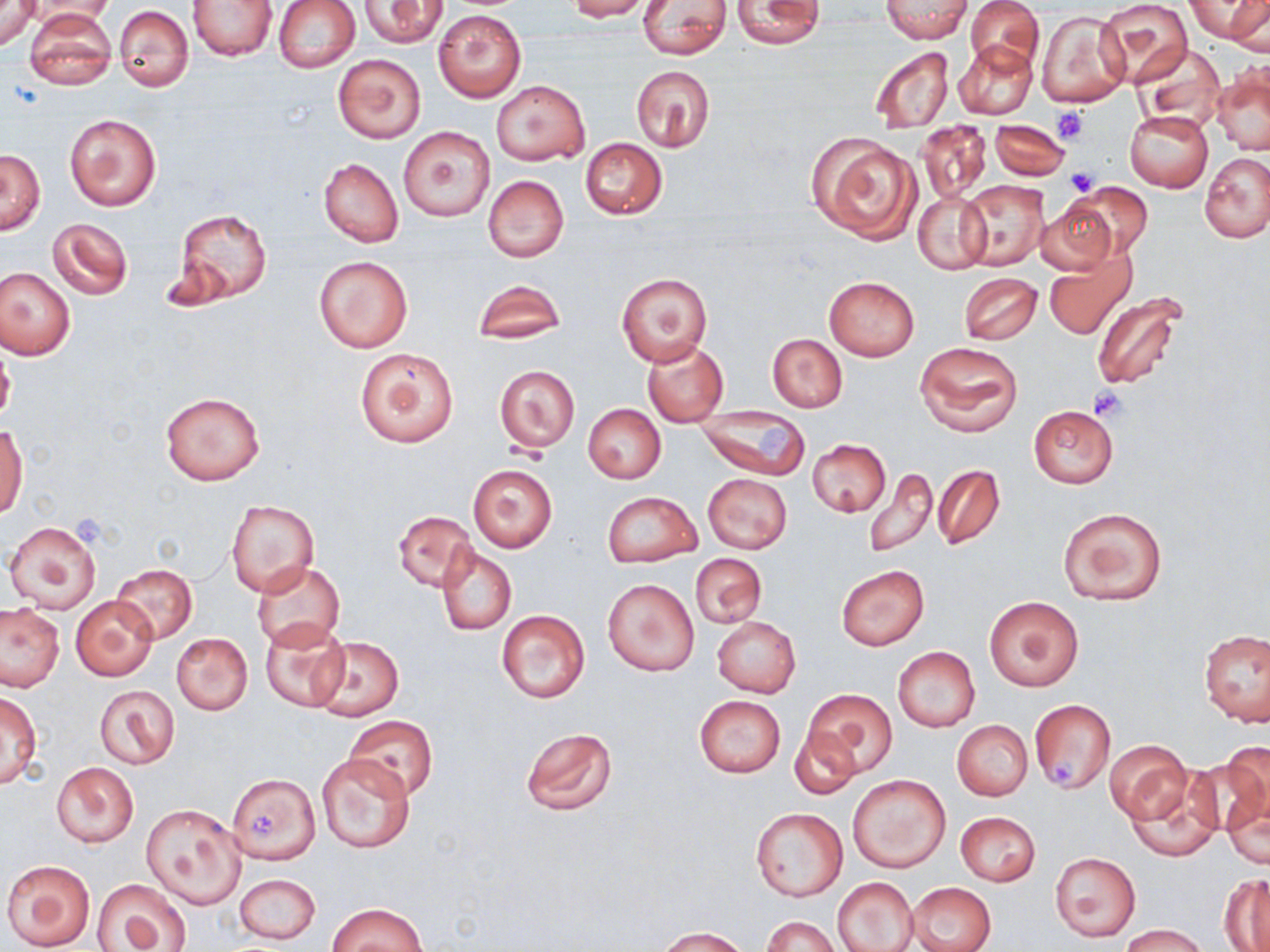
slide-level diagnosis = negative for blood parasites
modality = light microscopy
stain = May-Grünwald-Giemsa
platelet locations = approximate bounding boxes as named x1/y1/x2/y2 corners in pixels: (x1=1052, y1=106, x2=1088, y2=144), (x1=1065, y1=168, x2=1100, y2=195), (x1=1089, y1=385, x2=1129, y2=420), (x1=757, y1=426, x2=795, y2=465), (x1=1051, y1=762, x2=1078, y2=787), (x1=251, y1=814, x2=277, y2=837)
field of view = one of a larger specimen
magnification = 1000x
image size = 1270×952 pixels
preparation = thin blood film
uninfected red blood cell locations = approximate bounding boxes as named x1/y1/x2/y2 corners in pixels: (x1=0, y1=0, x2=39, y2=50), (x1=273, y1=0, x2=359, y2=72), (x1=567, y1=0, x2=652, y2=21), (x1=882, y1=0, x2=971, y2=42), (x1=967, y1=0, x2=1043, y2=72), (x1=1095, y1=0, x2=1193, y2=85), (x1=1187, y1=0, x2=1267, y2=43), (x1=1228, y1=0, x2=1269, y2=53), (x1=28, y1=1, x2=118, y2=26), (x1=189, y1=1, x2=276, y2=60), (x1=358, y1=1, x2=447, y2=47), (x1=638, y1=1, x2=732, y2=58), (x1=731, y1=2, x2=827, y2=49), (x1=114, y1=5, x2=194, y2=92), (x1=25, y1=9, x2=115, y2=89), (x1=434, y1=9, x2=526, y2=102), (x1=1036, y1=9, x2=1130, y2=109), (x1=954, y1=39, x2=1036, y2=120), (x1=1135, y1=42, x2=1226, y2=132), (x1=867, y1=46, x2=954, y2=135), (x1=333, y1=55, x2=424, y2=143), (x1=1211, y1=62, x2=1269, y2=158), (x1=629, y1=64, x2=715, y2=152), (x1=491, y1=80, x2=589, y2=166), (x1=1125, y1=111, x2=1213, y2=191), (x1=64, y1=112, x2=161, y2=212), (x1=989, y1=118, x2=1068, y2=181), (x1=917, y1=120, x2=992, y2=203), (x1=399, y1=127, x2=494, y2=221), (x1=808, y1=133, x2=922, y2=244), (x1=580, y1=138, x2=667, y2=219), (x1=1, y1=149, x2=45, y2=236), (x1=1200, y1=151, x2=1270, y2=243), (x1=319, y1=158, x2=403, y2=247), (x1=483, y1=176, x2=569, y2=262), (x1=957, y1=178, x2=1049, y2=270), (x1=1067, y1=182, x2=1152, y2=261), (x1=913, y1=191, x2=991, y2=274), (x1=1035, y1=201, x2=1117, y2=275), (x1=173, y1=209, x2=272, y2=306), (x1=48, y1=218, x2=133, y2=300), (x1=1044, y1=249, x2=1134, y2=340), (x1=314, y1=256, x2=412, y2=352), (x1=0, y1=268, x2=75, y2=360), (x1=959, y1=272, x2=1042, y2=345), (x1=617, y1=274, x2=712, y2=366), (x1=824, y1=276, x2=919, y2=360), (x1=471, y1=280, x2=567, y2=347), (x1=1089, y1=290, x2=1193, y2=394), (x1=768, y1=334, x2=846, y2=412), (x1=642, y1=341, x2=728, y2=425), (x1=916, y1=341, x2=1022, y2=437), (x1=355, y1=347, x2=459, y2=448), (x1=495, y1=365, x2=579, y2=453), (x1=159, y1=391, x2=265, y2=485), (x1=583, y1=404, x2=666, y2=484), (x1=1028, y1=406, x2=1118, y2=487), (x1=695, y1=408, x2=812, y2=480), (x1=0, y1=422, x2=27, y2=518), (x1=807, y1=439, x2=891, y2=516), (x1=467, y1=463, x2=557, y2=553), (x1=933, y1=464, x2=1005, y2=550), (x1=862, y1=466, x2=937, y2=557), (x1=703, y1=473, x2=793, y2=554), (x1=602, y1=490, x2=701, y2=567), (x1=227, y1=500, x2=319, y2=599), (x1=1057, y1=507, x2=1167, y2=607), (x1=392, y1=511, x2=478, y2=591), (x1=4, y1=521, x2=102, y2=613), (x1=437, y1=548, x2=516, y2=635), (x1=691, y1=554, x2=766, y2=629), (x1=253, y1=561, x2=345, y2=651), (x1=110, y1=565, x2=197, y2=644), (x1=836, y1=565, x2=930, y2=650), (x1=603, y1=577, x2=700, y2=676), (x1=985, y1=594, x2=1084, y2=692), (x1=71, y1=596, x2=157, y2=680), (x1=0, y1=604, x2=64, y2=691), (x1=496, y1=609, x2=590, y2=704), (x1=712, y1=616, x2=801, y2=697), (x1=260, y1=619, x2=349, y2=712), (x1=1199, y1=628, x2=1270, y2=725), (x1=171, y1=632, x2=253, y2=715), (x1=311, y1=637, x2=404, y2=721), (x1=892, y1=646, x2=980, y2=732), (x1=95, y1=685, x2=178, y2=769), (x1=804, y1=688, x2=897, y2=778), (x1=0, y1=691, x2=42, y2=787), (x1=694, y1=695, x2=786, y2=777), (x1=1030, y1=698, x2=1115, y2=793), (x1=1031, y1=700, x2=1116, y2=794), (x1=345, y1=717, x2=437, y2=801), (x1=953, y1=721, x2=1032, y2=801), (x1=519, y1=726, x2=618, y2=816), (x1=790, y1=727, x2=861, y2=799), (x1=1105, y1=739, x2=1191, y2=823), (x1=316, y1=752, x2=418, y2=855), (x1=1192, y1=752, x2=1269, y2=847), (x1=52, y1=762, x2=139, y2=848), (x1=1127, y1=772, x2=1222, y2=861), (x1=228, y1=773, x2=318, y2=863), (x1=847, y1=774, x2=951, y2=872), (x1=1221, y1=781, x2=1269, y2=869), (x1=141, y1=803, x2=244, y2=909), (x1=751, y1=808, x2=847, y2=901), (x1=955, y1=811, x2=1040, y2=886), (x1=1049, y1=852, x2=1141, y2=942), (x1=2, y1=858, x2=95, y2=951), (x1=233, y1=873, x2=321, y2=944), (x1=1220, y1=874, x2=1270, y2=952), (x1=834, y1=876, x2=919, y2=952), (x1=93, y1=877, x2=193, y2=952), (x1=908, y1=882, x2=995, y2=952), (x1=326, y1=902, x2=427, y2=952), (x1=762, y1=915, x2=837, y2=952), (x1=1122, y1=923, x2=1206, y2=952), (x1=657, y1=926, x2=749, y2=951)